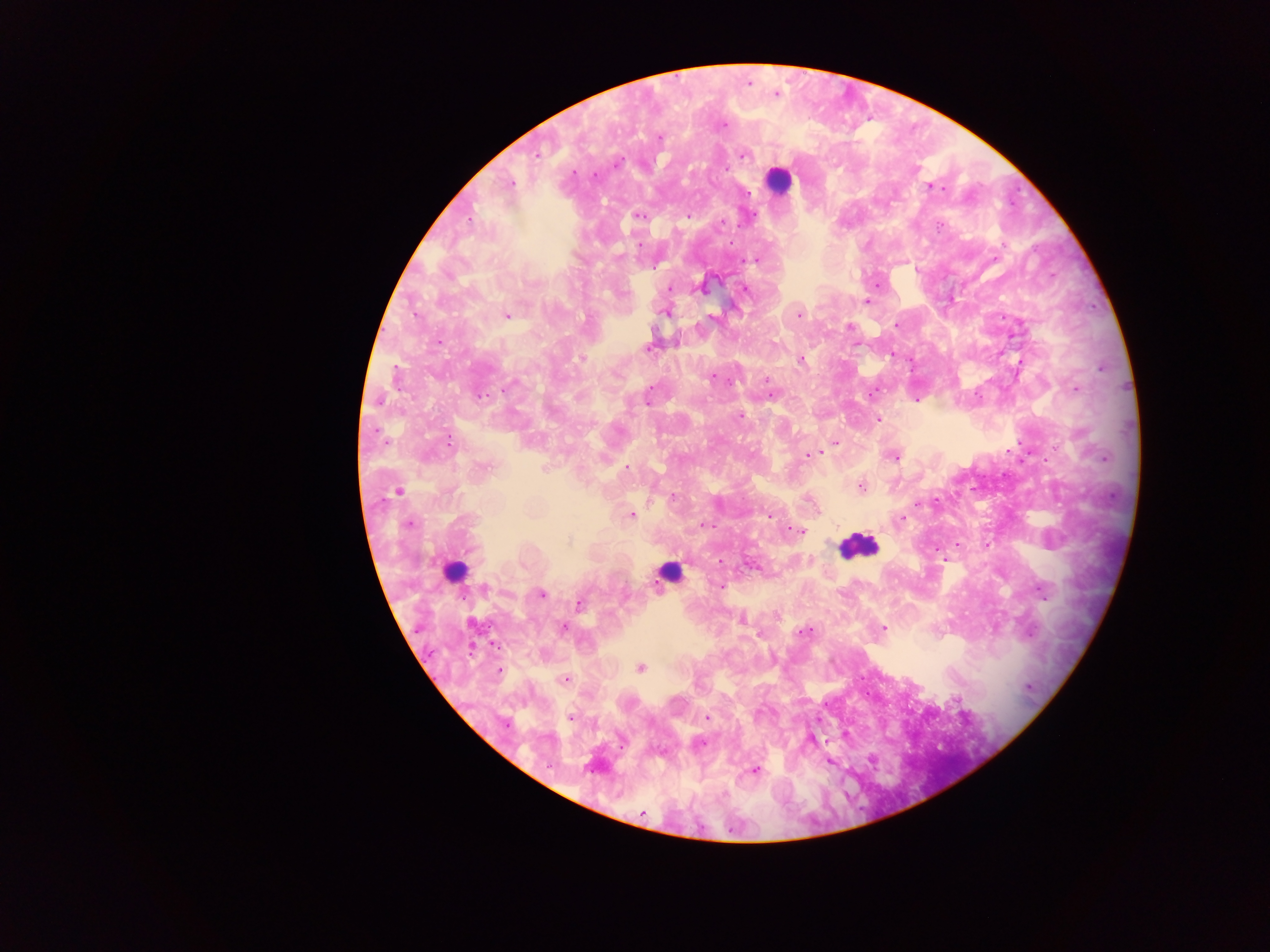

country = Ghana
image size = 1270×952 pixels
preparation = thick blood film
capture = mobile-phone photograph through a microscope
leukocyte locations = approximate centers as x y in pixels: 778 180; 858 546; 455 573; 669 576
Plasmodium parasite locations = approximate centers as x y in pixels: 748 83; 776 94; 724 126; 659 137; 743 155; 537 156; 617 163; 595 175; 510 184; 931 187; 937 187; 749 193; 639 216; 688 216; 469 220; 721 222; 939 226; 639 244; 755 260; 655 266; 670 288; 701 288; 744 289; 867 302; 665 312; 415 315; 506 315; 799 315; 711 317; 896 325; 850 327; 438 341; 678 343; 647 348; 891 355; 581 359; 801 360; 1101 369; 712 377; 767 380; 509 386; 1076 389; 772 395; 480 396; 378 400; 648 400; 740 416; 878 419; 836 442; 450 443; 821 451; 809 454; 894 457; 544 467; 627 468; 860 486; 398 491; 673 497; 918 503; 632 515; 768 516; 901 518; 409 524; 704 524; 798 532; 568 541; 987 546; 721 561; 752 566; 721 587; 485 589; 1041 590; 541 595; 579 605; 741 620; 564 628; 883 628; 804 632; 494 645; 640 668; 499 671; 566 679; 957 699; 571 717; 707 718; 506 725; 701 743; 829 762; 755 770; 724 794; 643 813
field of view = single